Name the cell type shown.
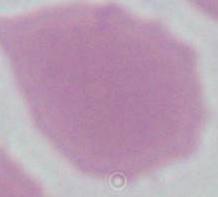

This is an erythrocyte.

Summary:
  - Magnification: 1000x
  - Modality: micrograph